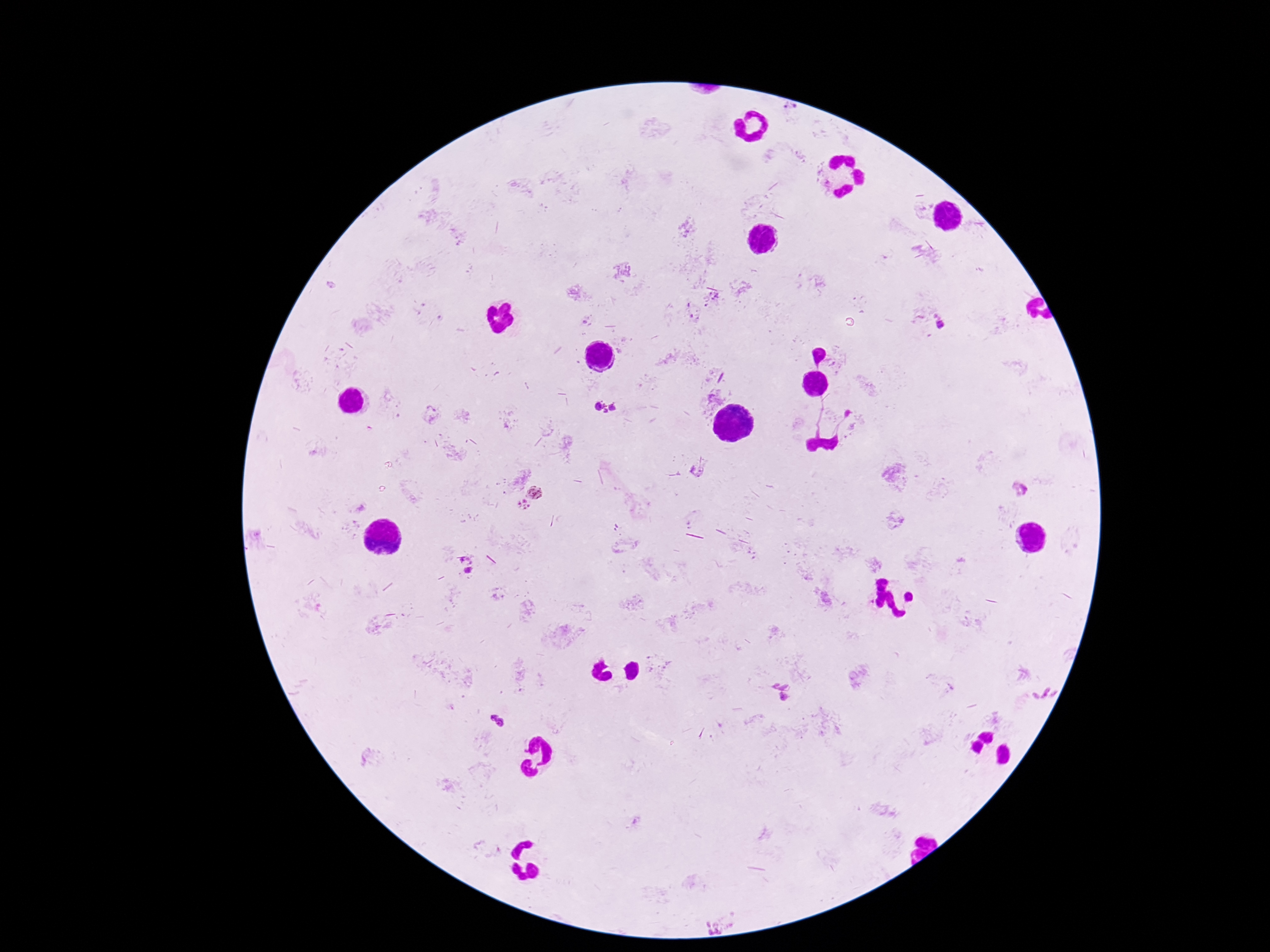
Approximate centers as [x, y] in pixels.
Summary:
  - Plasmodium parasite locations: [789, 109], [941, 326], [605, 407], [697, 472], [1020, 489], [535, 491], [523, 505], [466, 565], [782, 693], [1043, 694], [497, 720], [716, 926]
  - Preparation: thick blood film
  - Image size: 1270×952 pixels
  - Capture: smartphone camera through the microscope eyepiece
  - Field of view: one from this slide
  - Patient malaria status: positive
  - Stain: Giemsa
  - Magnification: 100x